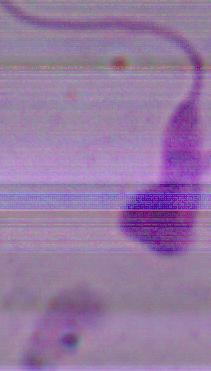
Captured at 1000x magnification. Micrograph. A Leishmania parasite is seen.